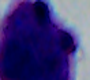
Summary:
  - Identification: white blood cell
  - Magnification: 1000x
  - Modality: photomicrograph